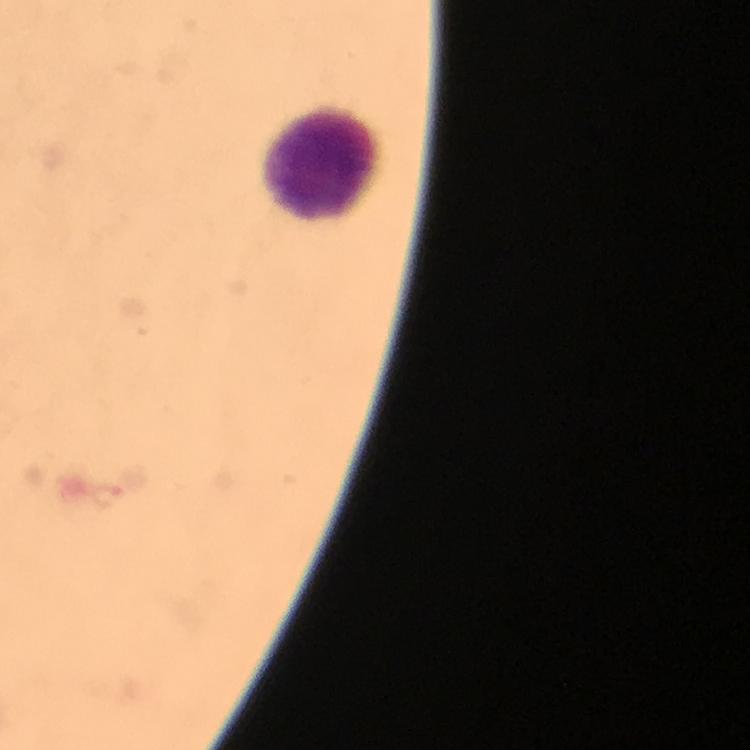
Approximate centers as [x, y] in pixels.
Summary:
  - Plasmodium parasite locations: [107, 496]
  - Leukocyte locations: [325, 165]
  - Immersion oil: used
  - Stain: Giemsa
  - Capture: smartphone camera through the microscope
  - Magnification: 100x
  - Image size: 750×750 pixels
  - Cropped from: a single field of view
  - Context: from a diagnostic examination for malaria
  - Preparation: thick blood film